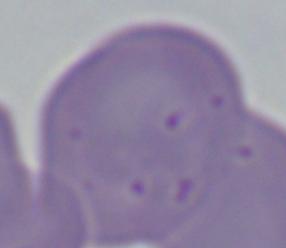
Summary:
  - Identification: Babesia
  - Modality: photomicrograph
  - Magnification: 1000x